Name the parasite shown.
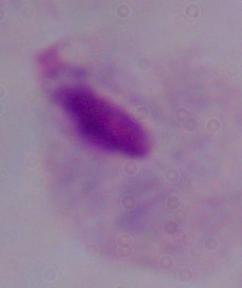

A trichomonad.

Photomicrograph. 1000x magnification.